Report the malaria status.
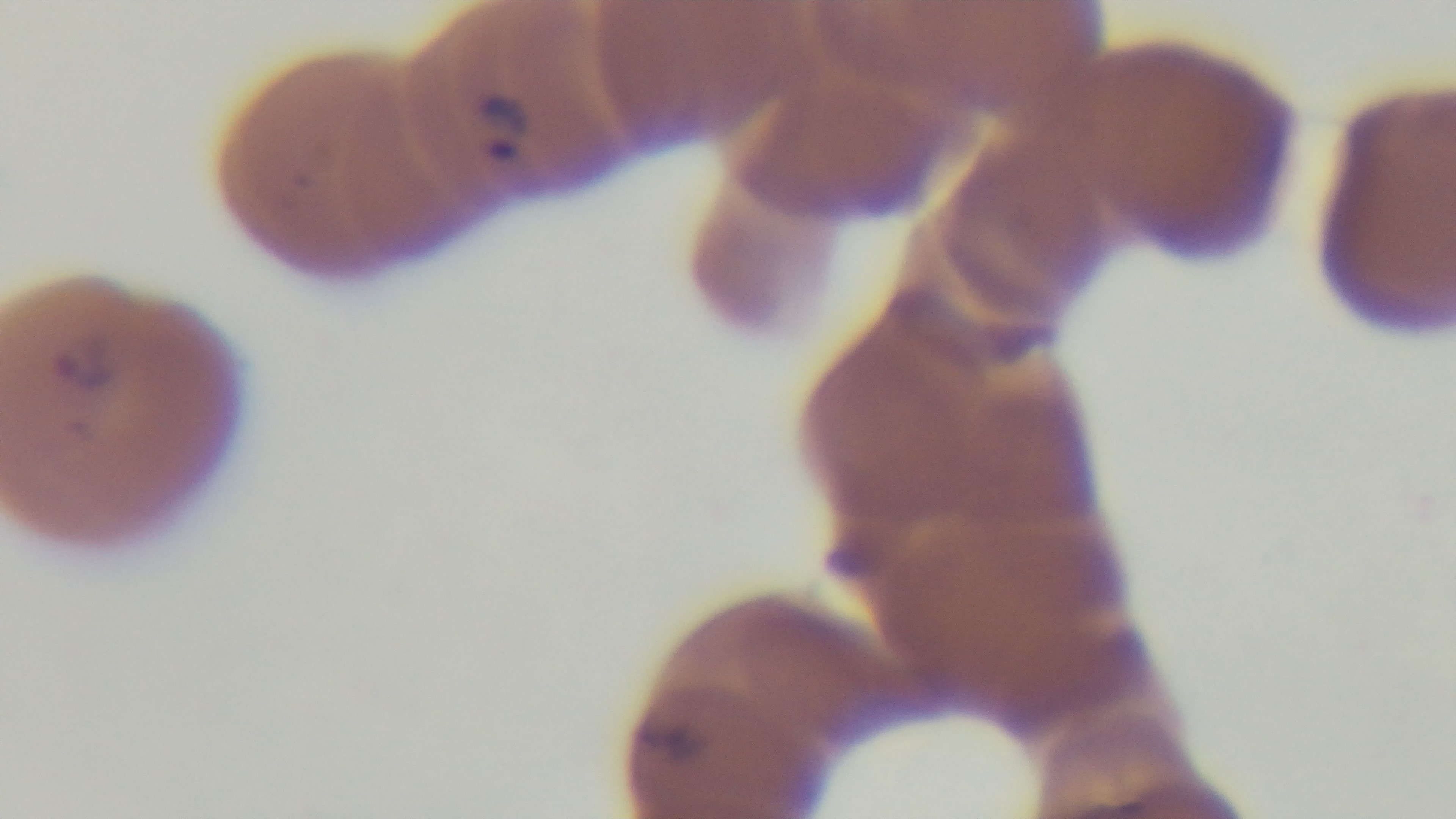
It is infected.

Preparation: thin blood film. Captured with a mounted 4K digital camera. Light microscopy. One field from the slide. 100x oil-immersion objective. Giemsa-stained.